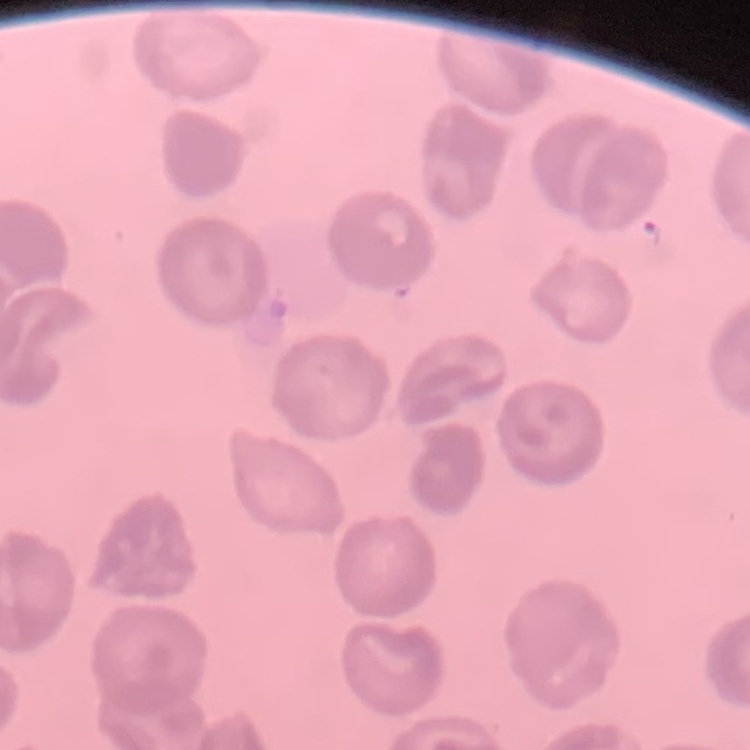
The red blood cells show no rouleaux formation. Thin blood film. Field's or Giemsa stain. One tile cut from a larger photomicrograph.